Classify this cell by malaria status.
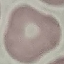

It is uninfected.

{
  "image_type": "automatically extracted cell patch, resized to 64 × 64 pixels",
  "preparation": "thin blood film",
  "capture": "smartphone camera at the microscope eyepiece",
  "stain": "Giemsa"
}